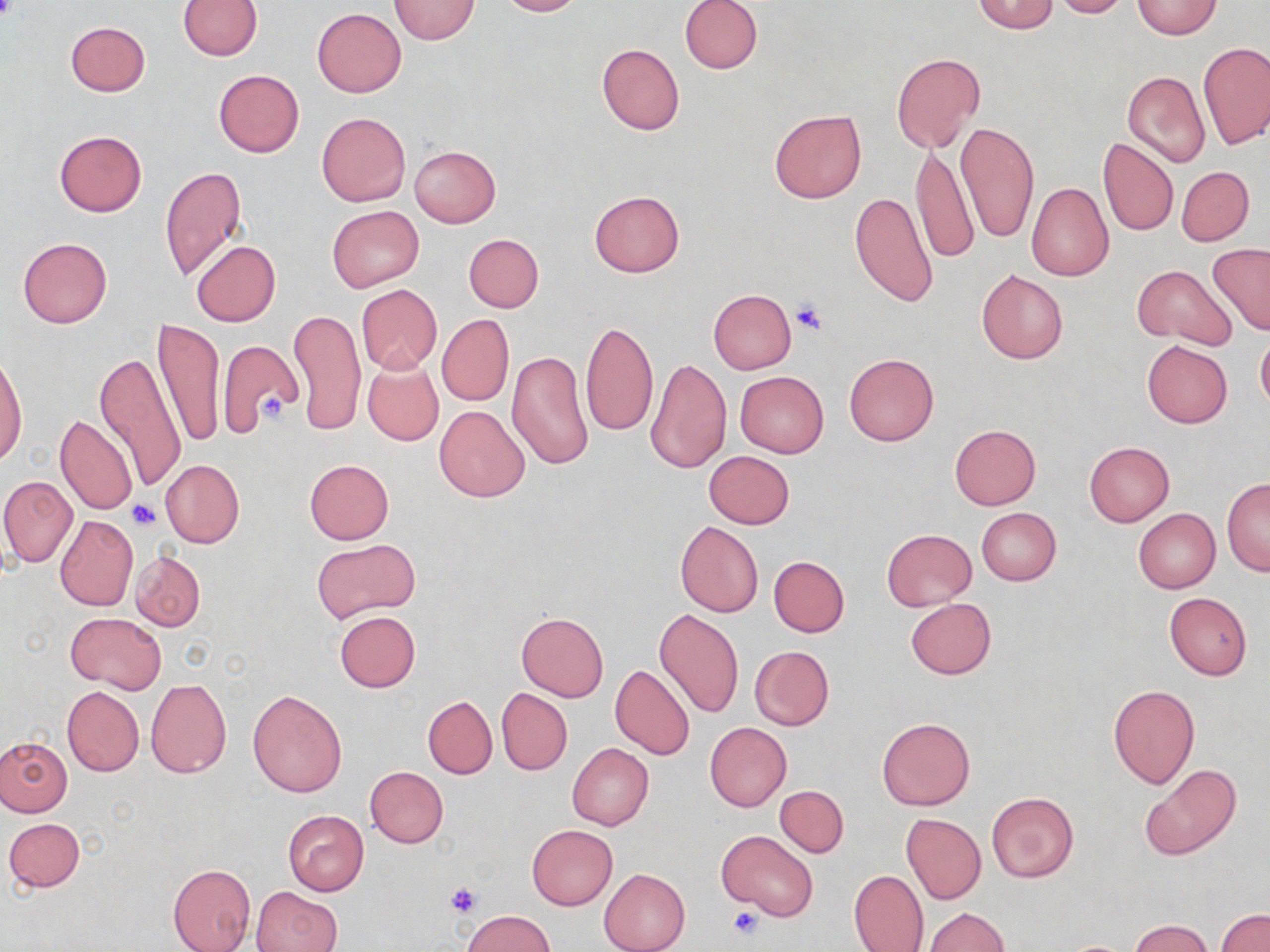

Summary:
  - Coordinate format: approximate bounding boxes as [x1, y1, x2, y2] in pixels
  - Platelet locations: [0, 0, 18, 25], [789, 298, 827, 333], [258, 392, 287, 424], [127, 499, 162, 530], [444, 882, 483, 918], [725, 904, 765, 942]
  - Uninfected red blood cell locations: [388, 0, 480, 45], [494, 0, 583, 16], [678, 0, 762, 74], [972, 0, 1060, 34], [1049, 0, 1130, 18], [178, 1, 262, 60], [1131, 1, 1223, 38], [312, 7, 406, 97], [65, 21, 149, 96], [1199, 42, 1270, 150], [597, 44, 684, 135], [891, 53, 986, 154], [213, 70, 304, 157], [1122, 71, 1210, 167], [769, 110, 868, 203], [316, 112, 410, 206], [954, 120, 1039, 245], [53, 130, 147, 216], [1098, 139, 1178, 236], [909, 143, 978, 266], [409, 145, 501, 227], [160, 165, 248, 280], [1176, 166, 1254, 246], [1027, 182, 1113, 281], [589, 191, 685, 277], [850, 192, 938, 307], [327, 205, 424, 293], [464, 234, 542, 312], [18, 238, 112, 327], [191, 241, 281, 326], [1207, 243, 1270, 338], [1131, 264, 1237, 350], [976, 270, 1068, 363], [356, 284, 442, 374], [708, 288, 795, 373], [289, 308, 366, 437], [437, 315, 514, 406], [155, 319, 224, 450], [581, 321, 658, 437], [1256, 333, 1270, 411], [1141, 340, 1232, 428], [217, 342, 304, 439], [507, 351, 592, 472], [0, 352, 27, 466], [94, 353, 187, 494], [844, 353, 938, 447], [645, 356, 731, 475], [361, 359, 443, 446], [735, 371, 828, 457], [434, 405, 529, 502], [55, 414, 137, 515], [949, 424, 1040, 509], [1083, 441, 1174, 527], [704, 451, 795, 529], [161, 460, 244, 547], [304, 460, 395, 544], [0, 475, 78, 568], [1222, 479, 1270, 576], [976, 507, 1062, 586], [1134, 509, 1220, 593], [54, 515, 138, 611], [676, 521, 763, 617], [882, 528, 977, 610], [313, 539, 420, 625], [131, 551, 206, 631], [768, 557, 849, 637], [1164, 593, 1251, 681], [905, 598, 996, 679], [654, 609, 744, 720], [335, 611, 420, 692], [515, 611, 607, 702], [65, 612, 166, 694], [749, 645, 835, 731], [609, 664, 695, 760], [145, 678, 232, 779], [1108, 685, 1199, 788], [62, 686, 144, 776], [247, 689, 347, 796], [497, 689, 572, 775], [423, 696, 497, 778], [877, 716, 975, 810], [705, 722, 792, 811], [0, 737, 72, 817], [567, 743, 653, 831], [1140, 764, 1242, 861], [365, 766, 448, 848], [775, 785, 849, 856], [986, 793, 1079, 882], [283, 811, 369, 895], [901, 813, 986, 904], [4, 817, 85, 892], [527, 825, 617, 910], [717, 830, 818, 921], [167, 863, 256, 952], [600, 868, 690, 952], [848, 870, 928, 952], [252, 886, 341, 952], [923, 907, 1009, 952], [1216, 909, 1270, 952], [462, 910, 554, 952], [1131, 919, 1213, 952]
  - Slide-level diagnosis: negative for blood parasites
  - Preparation: thin blood film
  - Modality: light microscopy
  - Field of view: one of a larger specimen
  - Magnification: 1000x
  - Image size: 1270×952 pixels
  - Stain: May-Grünwald-Giemsa